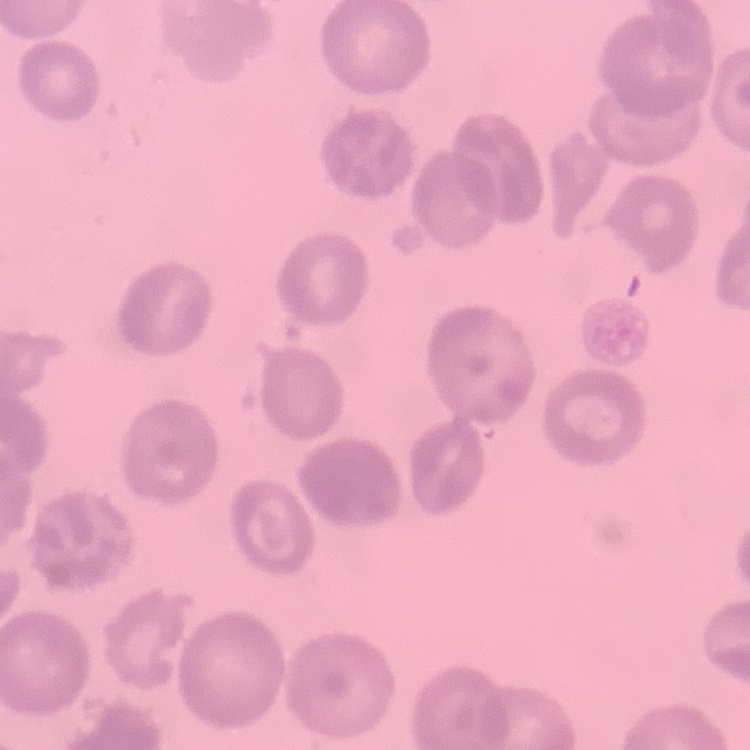 The red blood cells exhibit no rouleaux formation. Square crop of a larger photomicrograph. Thin blood smear. Stained with either Field's or Giemsa.